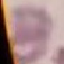

Summary:
  - Result: negative for malaria parasites
  - Capture: smartphone camera at the microscope eyepiece
  - Preparation: thin blood smear
  - Image type: automatically extracted cell patch, resized to 64 × 64 pixels
  - Stain: Giemsa